Report the malaria status of this cell.
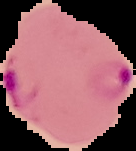

It is parasitized.

Summary:
  - Image type: segmented cell region with the area outside set to black
  - Image size: 136×151 pixels
  - Preparation: thin blood smear